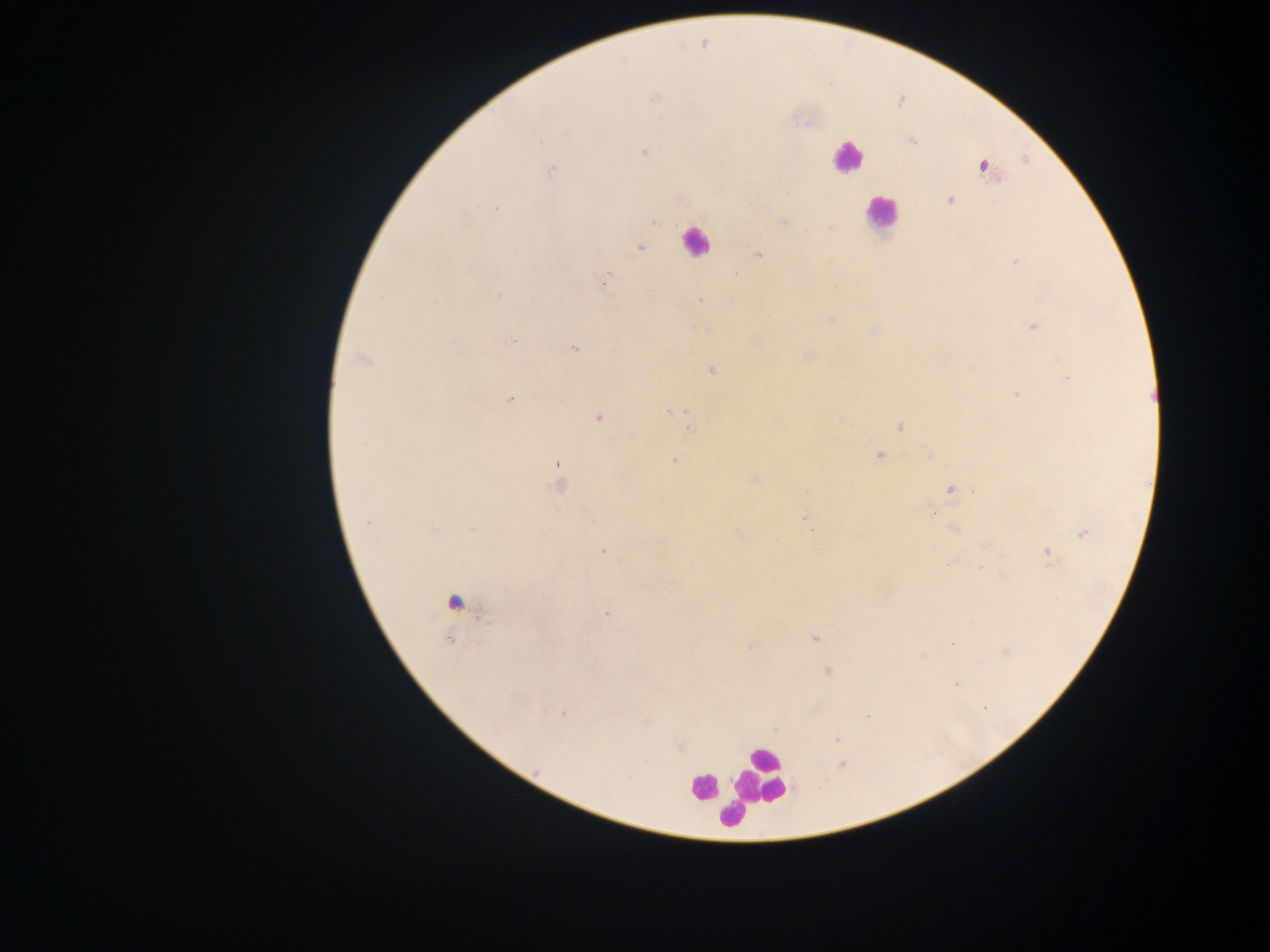

Approximate centers as [x, y] in pixels. Leukocyte locations: [847, 156], [880, 214], [695, 241], [456, 608], [762, 775], [702, 788], [730, 816]. Plasmodium parasite locations: [655, 97], [911, 141], [644, 152], [984, 166], [552, 170], [789, 192], [950, 200], [496, 207], [465, 217], [783, 221], [653, 222], [639, 247], [759, 254], [1015, 262], [606, 277], [700, 300], [1033, 326], [512, 340], [574, 349], [362, 358], [711, 370], [1067, 378], [1016, 394], [511, 398], [671, 412], [599, 417], [842, 420], [899, 427], [690, 428], [633, 436], [928, 452], [880, 455], [674, 461], [558, 472], [754, 478], [559, 485], [950, 489], [975, 491], [804, 518], [367, 523], [953, 528], [810, 529], [433, 530], [473, 530], [1083, 533], [987, 546], [603, 551], [1048, 553], [949, 562], [980, 569], [606, 612], [815, 638], [952, 643], [753, 645], [1006, 651], [828, 671], [955, 684], [983, 707], [563, 714], [867, 716], [645, 722], [837, 738], [645, 761], [842, 765], [537, 770]. Single field of view. Collected in Ghana. Thick blood smear. Mobile-phone photograph taken through the microscope. Image is 1270×952 pixels.